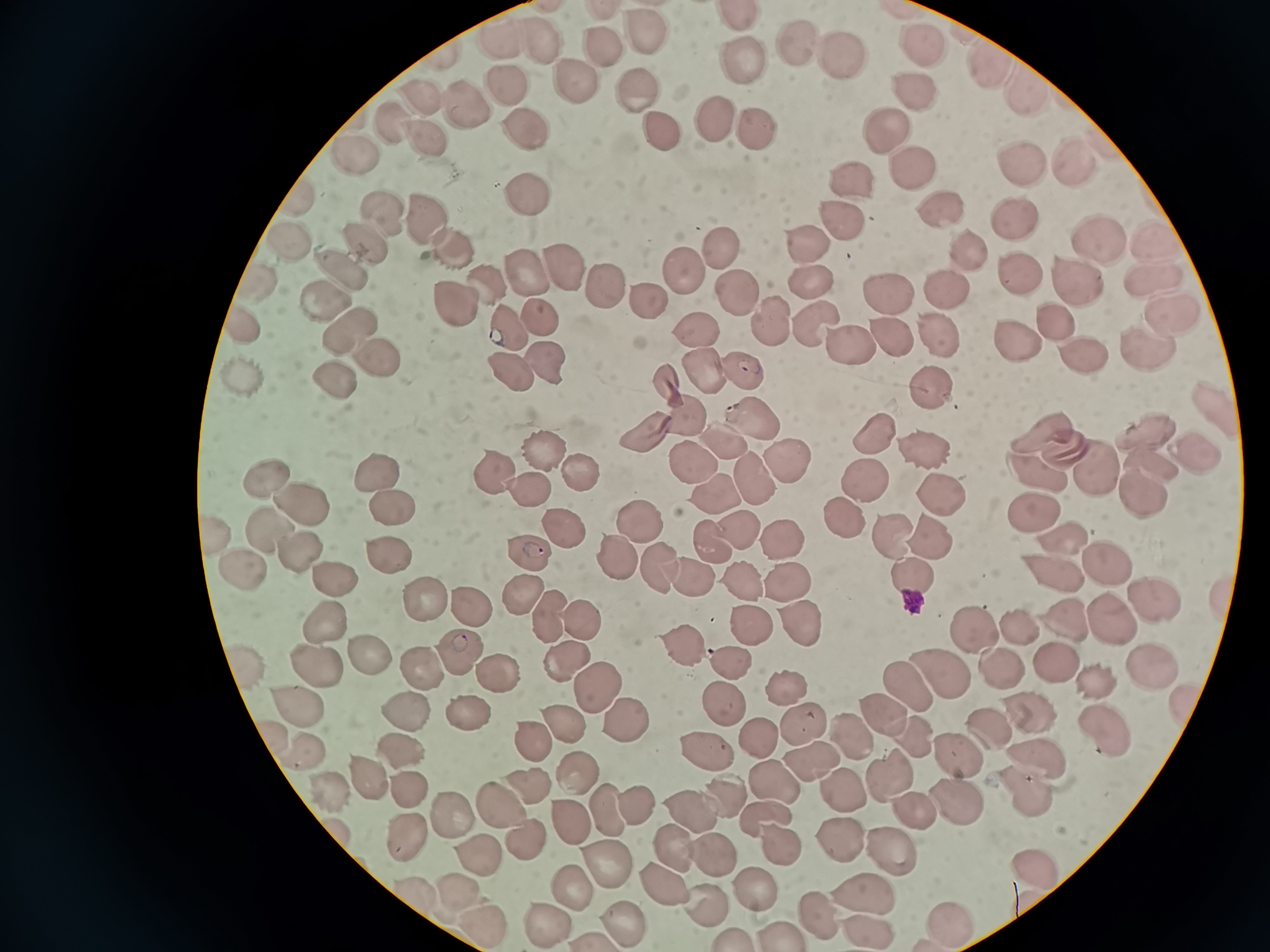 Approximate centers as {x, y} in pixels. Cell locations: {648, 37}, {500, 45}, {794, 45}, {593, 48}, {542, 50}, {835, 53}, {982, 64}, {742, 67}, {502, 85}, {575, 86}, {911, 88}, {1026, 93}, {420, 95}, {636, 96}, {456, 110}, {713, 116}, {393, 127}, {888, 128}, {524, 130}, {756, 132}, {661, 133}, {429, 138}, {353, 155}, {1068, 160}, {913, 163}, {1023, 164}, {851, 181}, {530, 200}, {938, 205}, {375, 210}, {421, 213}, {841, 218}, {1010, 219}, {808, 240}, {291, 242}, {454, 243}, {1154, 243}, {359, 244}, {1094, 247}, {724, 248}, {963, 250}, {566, 264}, {1015, 269}, {525, 270}, {334, 271}, {683, 271}, {807, 273}, {1076, 278}, {600, 279}, {490, 283}, {1149, 289}, {944, 291}, {253, 292}, {450, 294}, {737, 294}, {891, 297}, {645, 298}, {322, 302}, {1170, 312}, {545, 314}, {770, 317}, {1049, 319}, {808, 325}, {243, 329}, {345, 330}, {514, 331}, {693, 331}, {889, 332}, {939, 334}, {1006, 339}, {844, 344}, {1072, 345}, {1145, 349}, {379, 362}, {506, 365}, {542, 365}, {738, 368}, {699, 369}, {242, 370}, {329, 380}, {929, 388}, {1206, 407}, {684, 408}, {745, 415}, {636, 432}, {875, 432}, {718, 436}, {1141, 437}, {1046, 439}, {918, 445}, {538, 451}, {1186, 452}, {681, 457}, {779, 459}, {1147, 462}, {1086, 465}, {574, 467}, {377, 469}, {490, 472}, {1034, 472}, {270, 473}, {754, 473}, {860, 476}, {707, 487}, {933, 491}, {1135, 493}, {527, 494}, {301, 499}, {1027, 502}, {387, 506}, {839, 514}, {263, 520}, {637, 521}, {732, 526}, {883, 527}, {559, 530}, {1056, 534}, {925, 536}, {706, 539}, {779, 541}, {292, 545}, {1102, 552}, {384, 554}, {609, 555}, {525, 557}, {651, 564}, {237, 567}, {1056, 571}, {898, 573}, {782, 575}, {686, 576}, {741, 576}, {330, 580}, {517, 592}, {1152, 596}, {423, 598}, {464, 608}, {544, 613}, {1063, 614}, {323, 615}, {584, 616}, {801, 619}, {1111, 619}, {1015, 622}, {745, 624}, {977, 633}, {679, 641}, {561, 652}, {367, 655}, {455, 656}, {311, 658}, {727, 661}, {245, 662}, {420, 664}, {1153, 666}, {1057, 667}, {1000, 668}, {941, 673}, {488, 674}, {590, 676}, {910, 681}, {1100, 682}, {781, 687}, {618, 706}, {408, 709}, {882, 709}, {294, 710}, {474, 711}, {721, 711}, {566, 713}, {1024, 713}, {797, 721}, {1098, 725}, {987, 730}, {752, 731}, {845, 732}, {539, 737}, {908, 738}, {401, 745}, {955, 756}, {703, 757}, {306, 759}, {1036, 759}, {813, 762}, {576, 770}, {374, 776}, {885, 776}, {532, 783}, {774, 783}, {409, 785}, {1021, 785}, {336, 789}, {844, 790}, {951, 796}, {505, 803}, {630, 805}, {602, 806}, {907, 806}, {691, 813}, {762, 813}, {563, 817}, {405, 829}, {524, 830}, {833, 839}, {778, 844}, {666, 847}, {708, 850}, {485, 851}, {887, 851}, {1028, 862}, {600, 863}, {663, 884}, {574, 886}, {418, 888}, {744, 888}, {457, 891}, {856, 892}, {697, 898}, {816, 914}, {945, 919}, {481, 920}, {540, 921}, {618, 922}, {866, 926}, {773, 928}, {730, 932}. Thin blood smear. Giemsa stain. Image is 1270×952 pixels. Acquired by smartphone through the microscope eyepiece. One field from this slide.